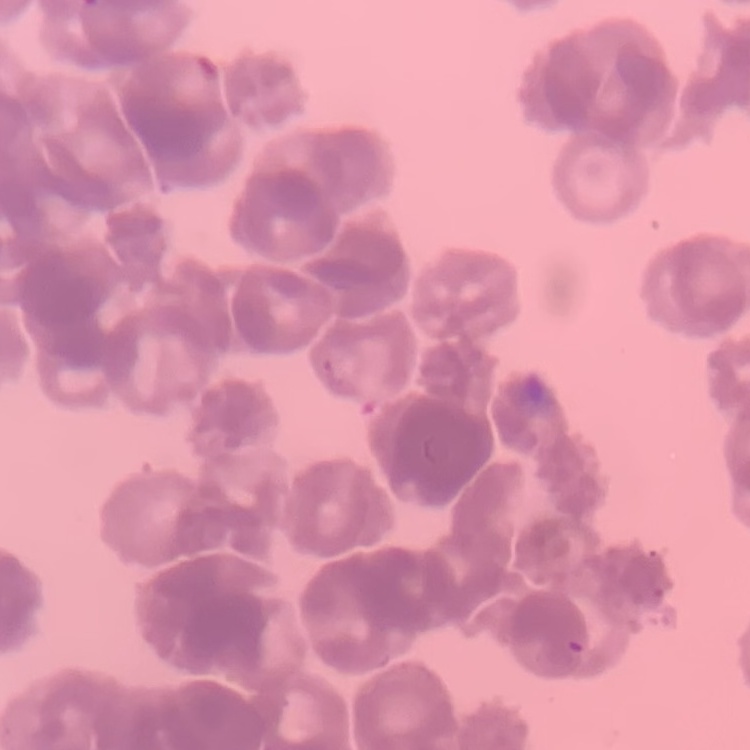

Summary:
  - Red blood cell morphology: rouleaux formation
  - Stain: Field's or Giemsa
  - Preparation: thin blood film
  - Image type: square crop of a larger photomicrograph